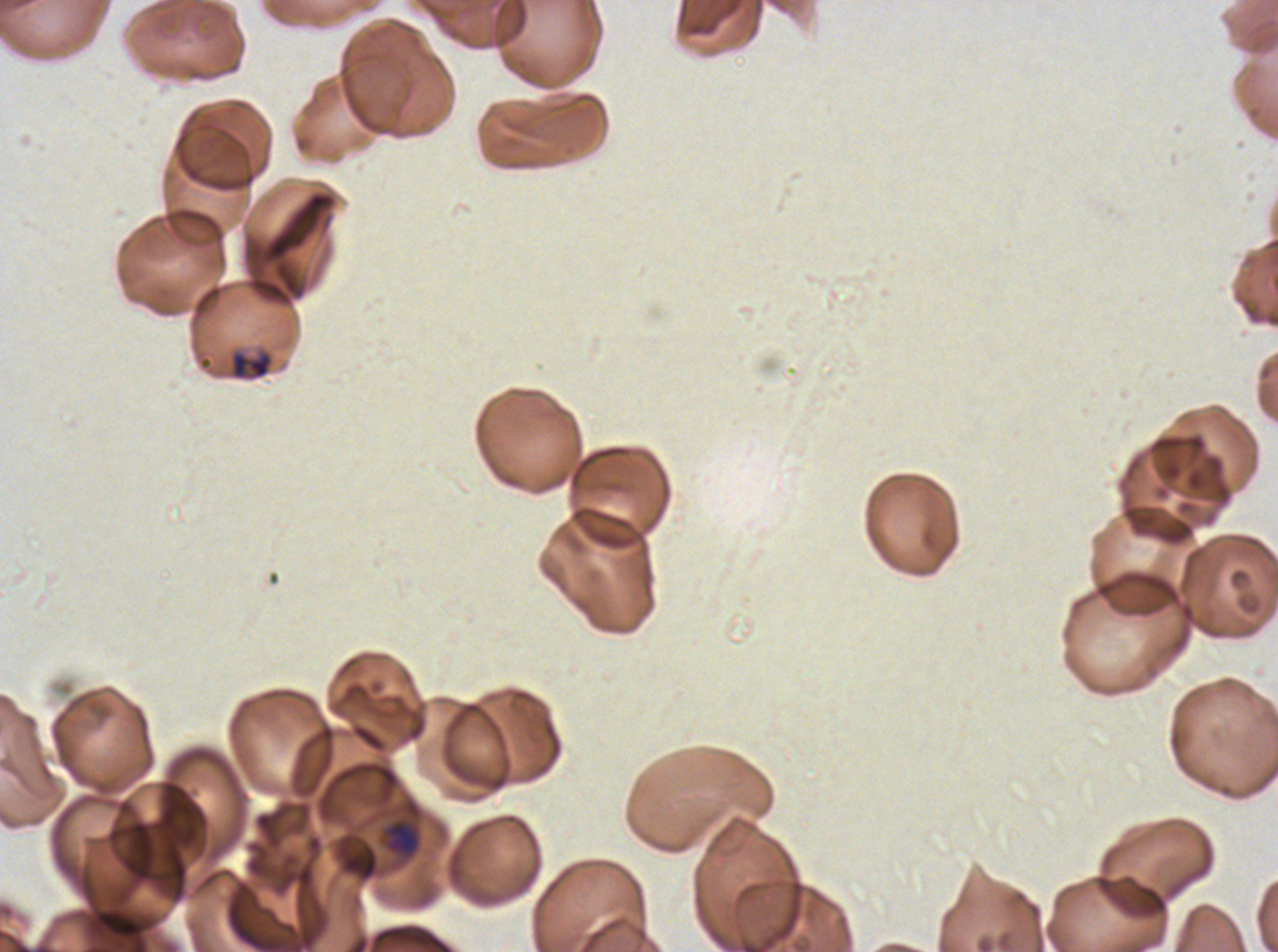
Approximate bounding boxes as [x1, y1, x2, y2] in pixels.
Summary:
  - Late-ring/early-trophozoite locations: [361, 857, 377, 879]
  - Mid trophozoite locations: [228, 348, 274, 382]
  - Image size: 1278×952 pixels
  - Stain: Giemsa
  - Life-cycle stages observed: late-ring/early-trophozoite, mid trophozoite
  - Field of view: one sub-image of a larger composite
  - Specimen: P. falciparum from a patient in The Gambia, cultured ex vivo for 24 to 48 hours
  - Preparation: thin blood smear